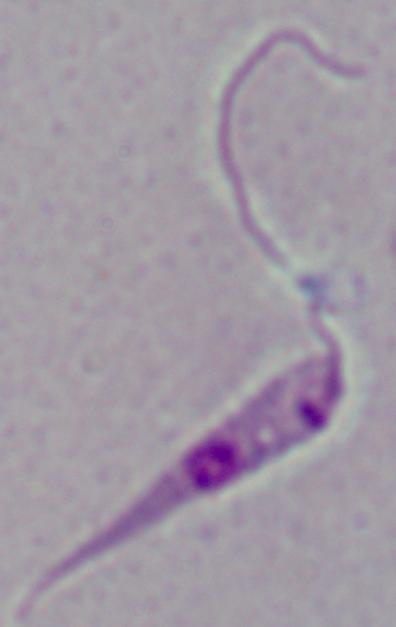

Summary:
  - Magnification: 1000x
  - Modality: photomicrograph
  - Identification: Leishmania